Locate and identify every blood parasite.
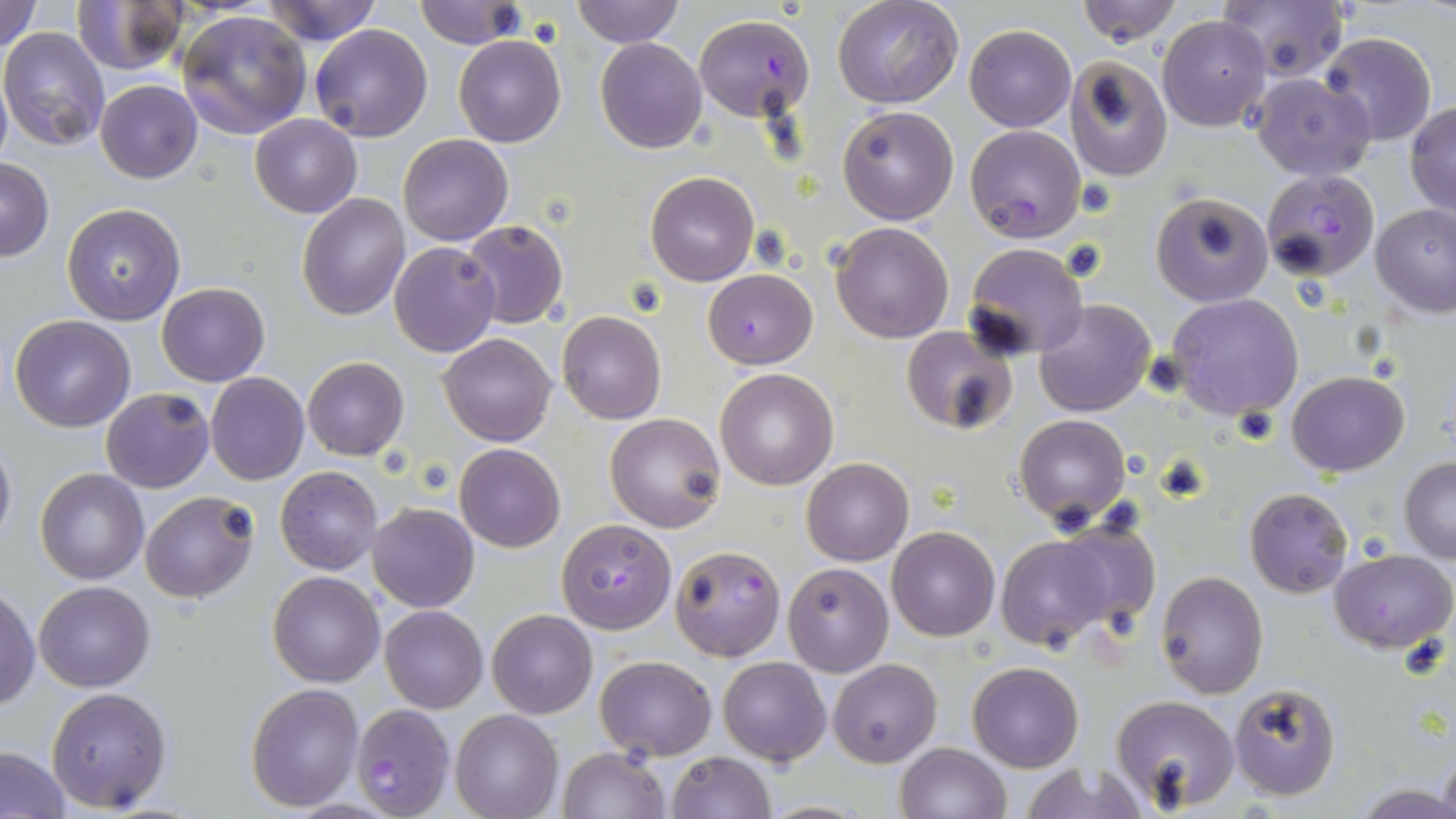

Approximate bounding boxes as (x1,y1)-(x2,y2) corner pairs in pixels.
Plasmodium falciparum-infected red blood cells: (694,15)-(817,122), (965,124)-(1085,242), (1260,168)-(1379,281), (556,519)-(677,635), (669,544)-(785,660), (351,704)-(453,818).
No Plasmodium ovale, Plasmodium malariae, Plasmodium vivax, Babesia divergens, or Trypanosoma brucei observed.

slide_level_diagnosis: Plasmodium falciparum
uninfected_red_blood_cell_locations: 'approximate bounding boxes as (x1,y1)-(x2,y2) corner pairs in pixels: (259,0)-(384,47), (414,0)-(525,49), (570,0)-(684,49), (833,0)-(964,108), (1076,0)-(1181,46), (0,1)-(41,52), (73,1)-(187,75), (1218,1)-(1346,81), (177,10)-(312,139), (1158,13)-(1270,130), (309,24)-(433,142), (964,25)-(1076,131), (0,27)-(112,151), (1318,32)-(1437,147), (455,35)-(564,147), (596,38)-(707,154), (1065,55)-(1172,182), (0,68)-(12,172), (1250,71)-(1378,182), (95,80)-(202,183), (1406,102)-(1456,218), (837,105)-(960,225), (250,114)-(361,218), (398,134)-(512,245), (1,157)-(54,260), (646,172)-(759,286), (1151,192)-(1273,307), (297,193)-(410,319), (62,203)-(185,325), (1369,203)-(1456,317), (461,219)-(569,330), (830,221)-(955,344), (390,241)-(501,356), (962,243)-(1089,360), (703,270)-(817,369), (157,282)-(269,385), (1166,293)-(1305,423), (1034,298)-(1157,417), (556,311)-(667,425), (9,314)-(137,432), (900,324)-(1019,436), (439,332)-(556,447), (301,356)-(408,460), (714,367)-(838,490), (1286,371)-(1410,476), (205,372)-(309,484), (101,388)-(213,492), (603,412)-(727,532), (1013,413)-(1132,529), (0,435)-(16,553), (455,443)-(565,551), (802,458)-(914,566), (1398,458)-(1456,564), (276,466)-(382,575), (36,468)-(149,584), (1244,487)-(1353,598), (140,492)-(258,603), (368,502)-(479,611), (1049,518)-(1163,637), (886,527)-(1000,641), (993,530)-(1127,651), (1330,548)-(1455,655), (783,562)-(894,676), (267,570)-(385,688), (1156,570)-(1267,697), (34,580)-(156,692), (0,586)-(39,711), (379,606)-(488,713), (487,609)-(597,719), (595,654)-(716,760), (717,655)-(831,766), (827,658)-(941,768), (968,662)-(1082,772), (245,682)-(363,810), (1229,683)-(1340,801), (46,686)-(172,812), (1110,695)-(1239,812), (450,710)-(562,819), (895,742)-(1012,819), (0,746)-(71,816), (557,747)-(670,819), (1438,747)-(1456,819), (666,751)-(775,819), (1018,760)-(1148,819), (1360,785)-(1456,817)'
platelet_locations: 'approximate bounding boxes as (x1,y1)-(x2,y2) corner pairs in pixels: (1077,176)-(1118,217)'
magnification: 1000x
image_size: 1456×819 pixels
modality: optical microscopy
preparation: thin blood smear
field_of_view: one of a larger specimen
stain: May-Grünwald-Giemsa